Point out leukocytes.
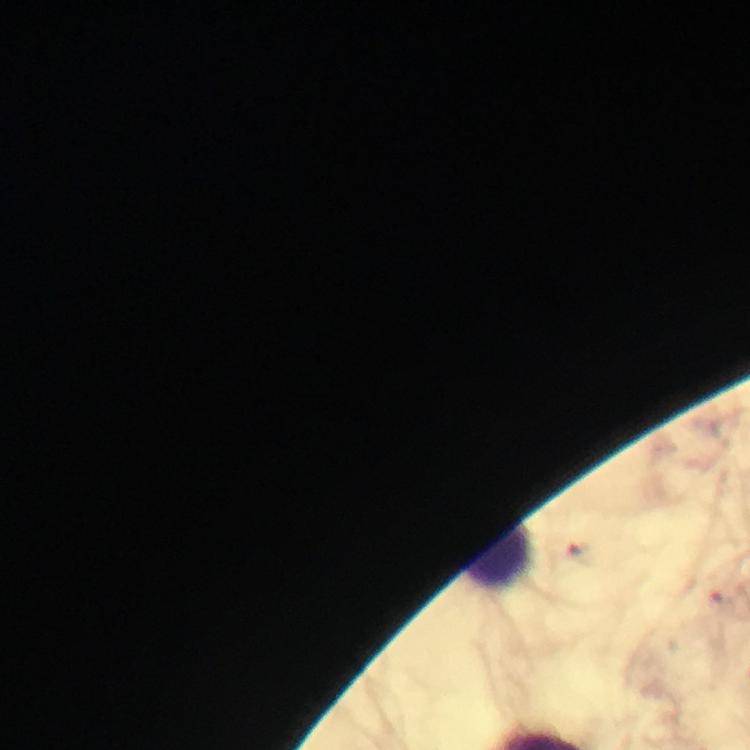
Approximate centers as [x, y] in pixels.
Leukocytes: [497, 557].

Thick blood film. Photographed with a smartphone mounted on the microscope. Immersion oil was used. Giemsa-stained preparation. 100x magnification. From a malaria diagnostic workup. Cropped region of a single field of view. Plasmodium parasites: none detected. Image is 750×750 pixels.